Assess for malaria.
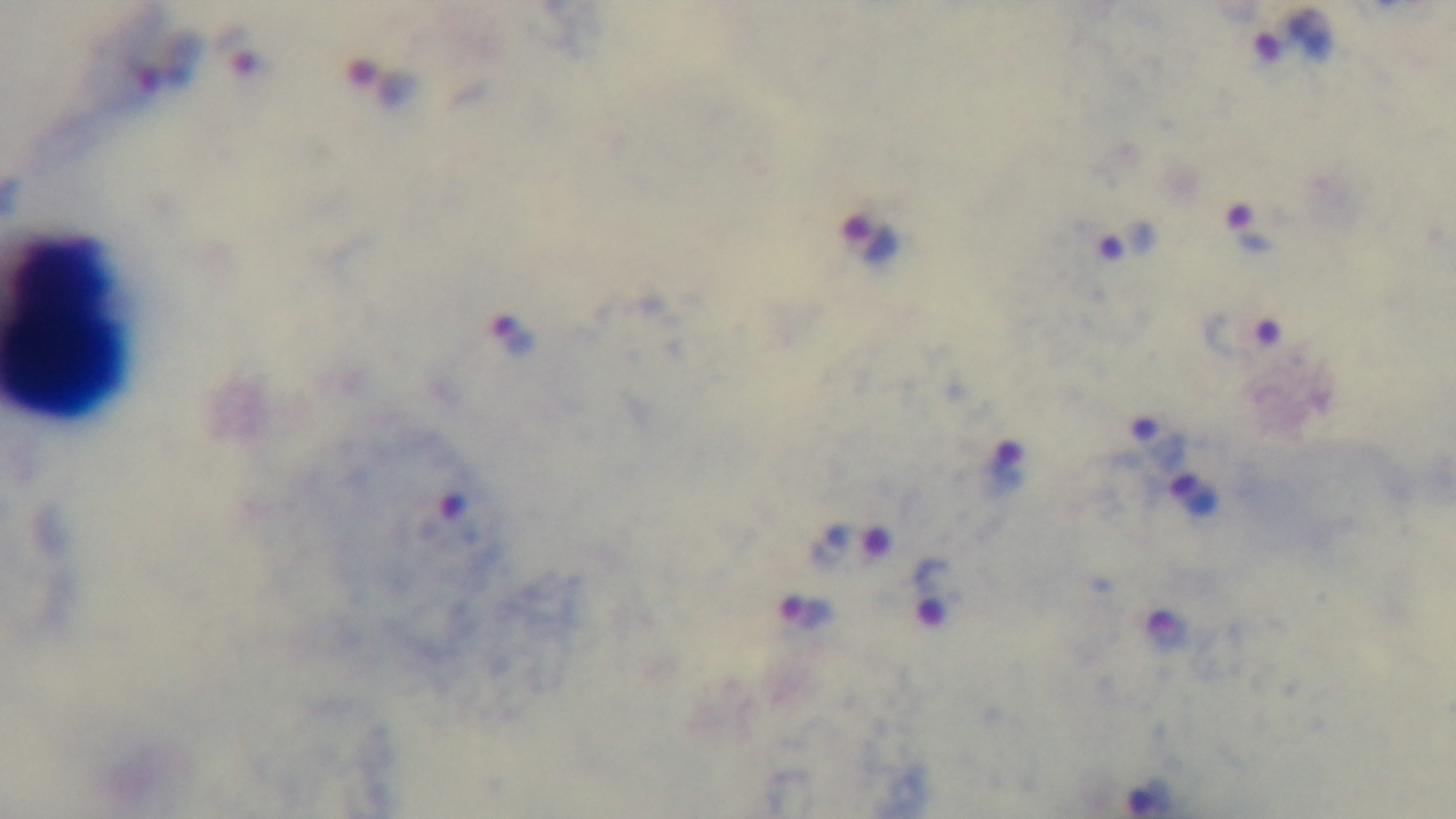

It is infected.

One field from the slide. Preparation: thick. Photomicrograph. Mounted 4K digital camera. Oil-immersion objective, 100x. Giemsa stain.